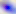

Summary:
  - Modality: micrograph
  - Magnification: 400x
  - Identification: Toxoplasma gondii